Locate and identify every blood parasite.
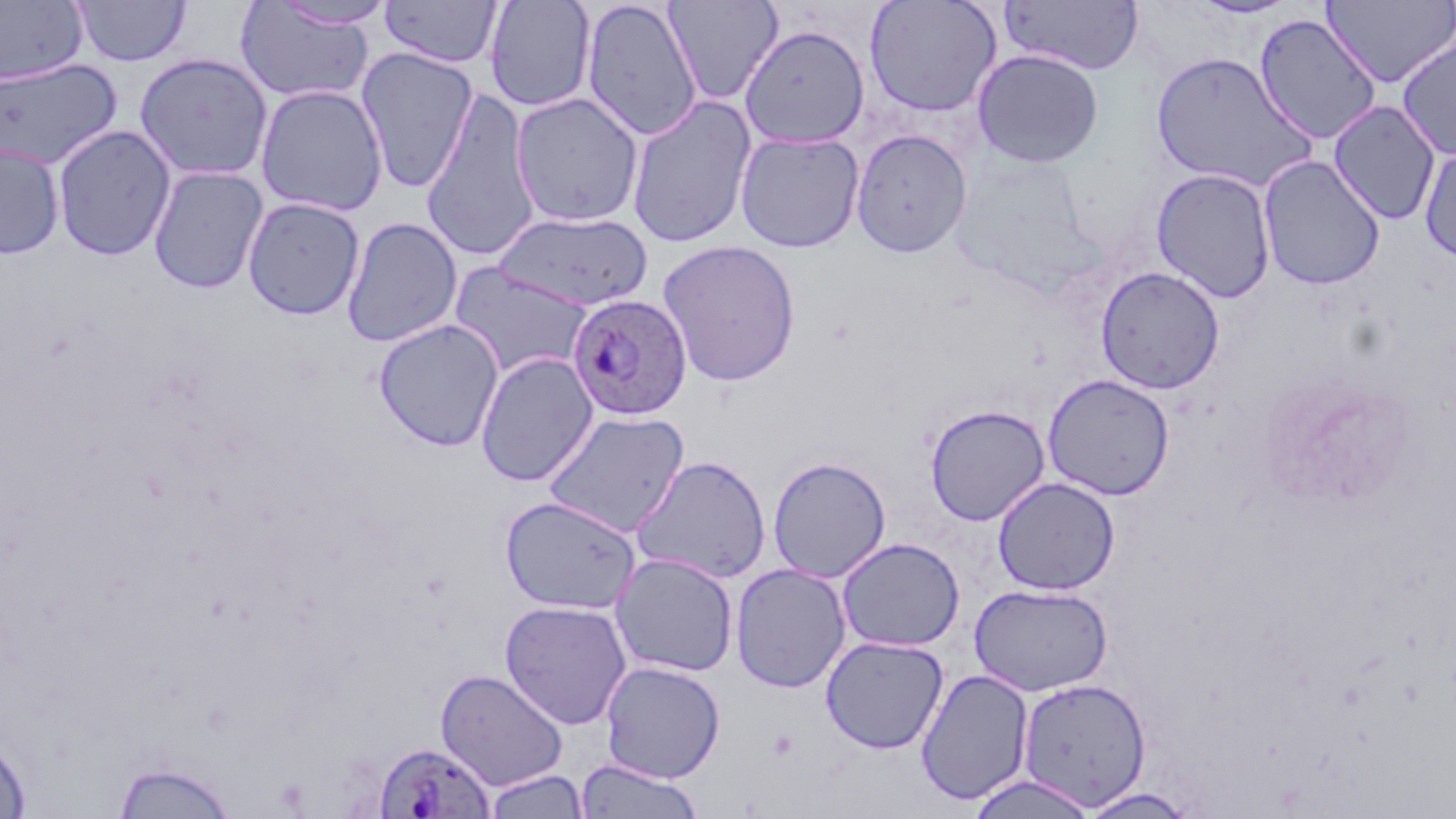
Approximate bounding boxes as (x1,y1)-(x2,y2) corner pairs in pixels.
Plasmodium ovale-infected red blood cells: (567,293)-(692,420), (372,741)-(495,818).
No Plasmodium falciparum, Plasmodium malariae, Plasmodium vivax, Babesia divergens, or Trypanosoma brucei observed.

slide_level_diagnosis: Plasmodium ovale
stain: May-Grünwald-Giemsa
uninfected_red_blood_cell_locations: 'approximate bounding boxes as (x1,y1)-(x2,y2) corner pairs in pixels: (379,0)-(503,68), (484,0)-(596,112), (580,0)-(702,141), (663,0)-(783,105), (864,0)-(1003,118), (1322,0)-(1456,88), (0,1)-(87,85), (72,1)-(192,67), (271,1)-(398,29), (999,1)-(1144,75), (234,2)-(376,105), (1253,13)-(1383,145), (738,24)-(871,148), (1396,33)-(1456,161), (356,47)-(479,191), (971,48)-(1105,168), (1149,51)-(1318,192), (134,53)-(273,181), (0,58)-(121,170), (255,84)-(388,217), (420,88)-(541,261), (509,92)-(645,228), (626,95)-(758,249), (1327,100)-(1442,225), (52,124)-(176,262), (850,129)-(972,258), (734,131)-(865,253), (0,142)-(65,259), (1419,143)-(1456,265), (1258,155)-(1386,290), (148,165)-(268,294), (1151,168)-(1277,303), (242,196)-(365,320), (492,211)-(654,311), (341,216)-(462,348), (657,240)-(801,387), (449,263)-(594,380), (1095,266)-(1225,394), (374,318)-(504,452), (476,352)-(598,486), (1041,373)-(1175,501), (924,404)-(1050,526), (542,410)-(691,537), (631,454)-(771,584), (768,456)-(891,583), (992,477)-(1120,596), (499,495)-(641,615), (836,537)-(965,652), (610,552)-(739,678), (730,563)-(851,693), (969,583)-(1113,696), (499,600)-(632,729), (820,635)-(949,754), (600,661)-(726,782), (435,668)-(567,791), (915,668)-(1034,805), (1017,677)-(1151,809), (0,735)-(31,818), (111,758)-(237,818), (574,759)-(706,819), (483,770)-(590,818), (966,773)-(1098,818), (1075,787)-(1202,818)'
image_size: 1456×819 pixels
magnification: 1000x
field_of_view: single
preparation: thin blood film
modality: light microscopy